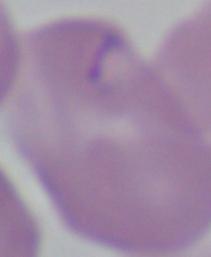

Summary:
  - Magnification: 1000x
  - Modality: micrograph
  - Identification: Babesia